Identify the parasite.
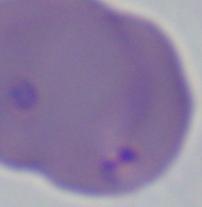
This is Babesia.

Micrograph. Captured at 1000x magnification.